State which parasite is depicted.
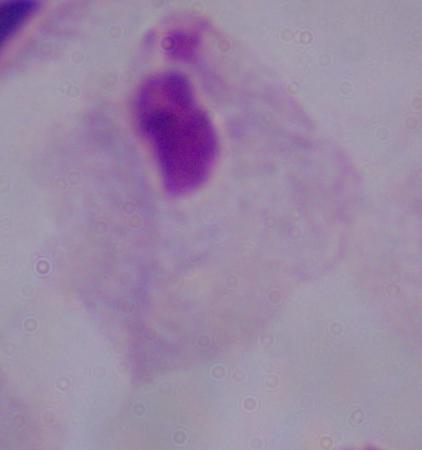
This is a trichomonad.

Captured at 1000x magnification. Micrograph.